Assess the morphology of the red blood cells.
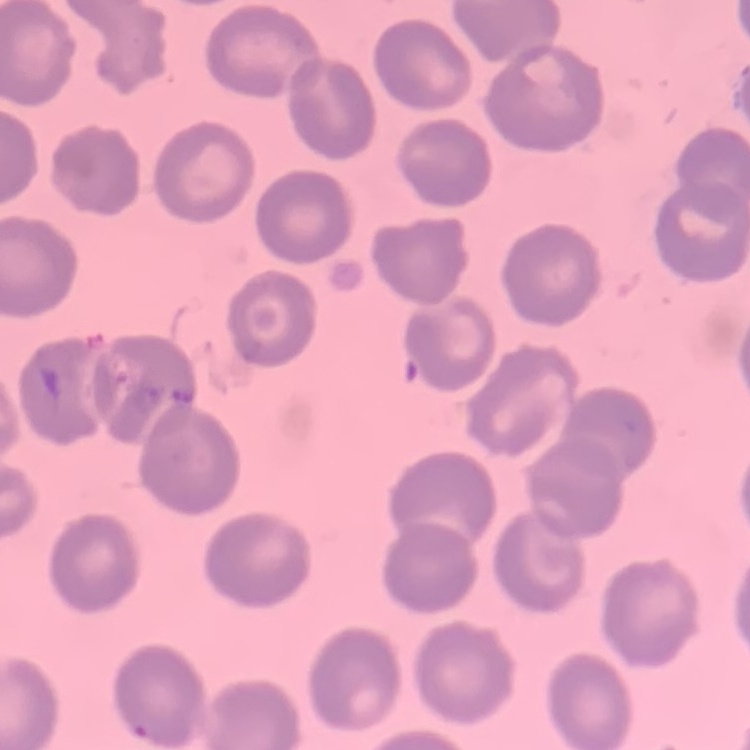

They show no rouleaux formation.

Summary:
  - Preparation: thin blood smear
  - Stain: Field's or Giemsa
  - Image type: one tile cut from a larger photomicrograph